Report the malaria status of this cell.
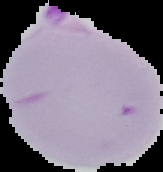
Parasitized.

image size = 163×172 pixels
preparation = thin blood film
image type = segmented cell region on a black background